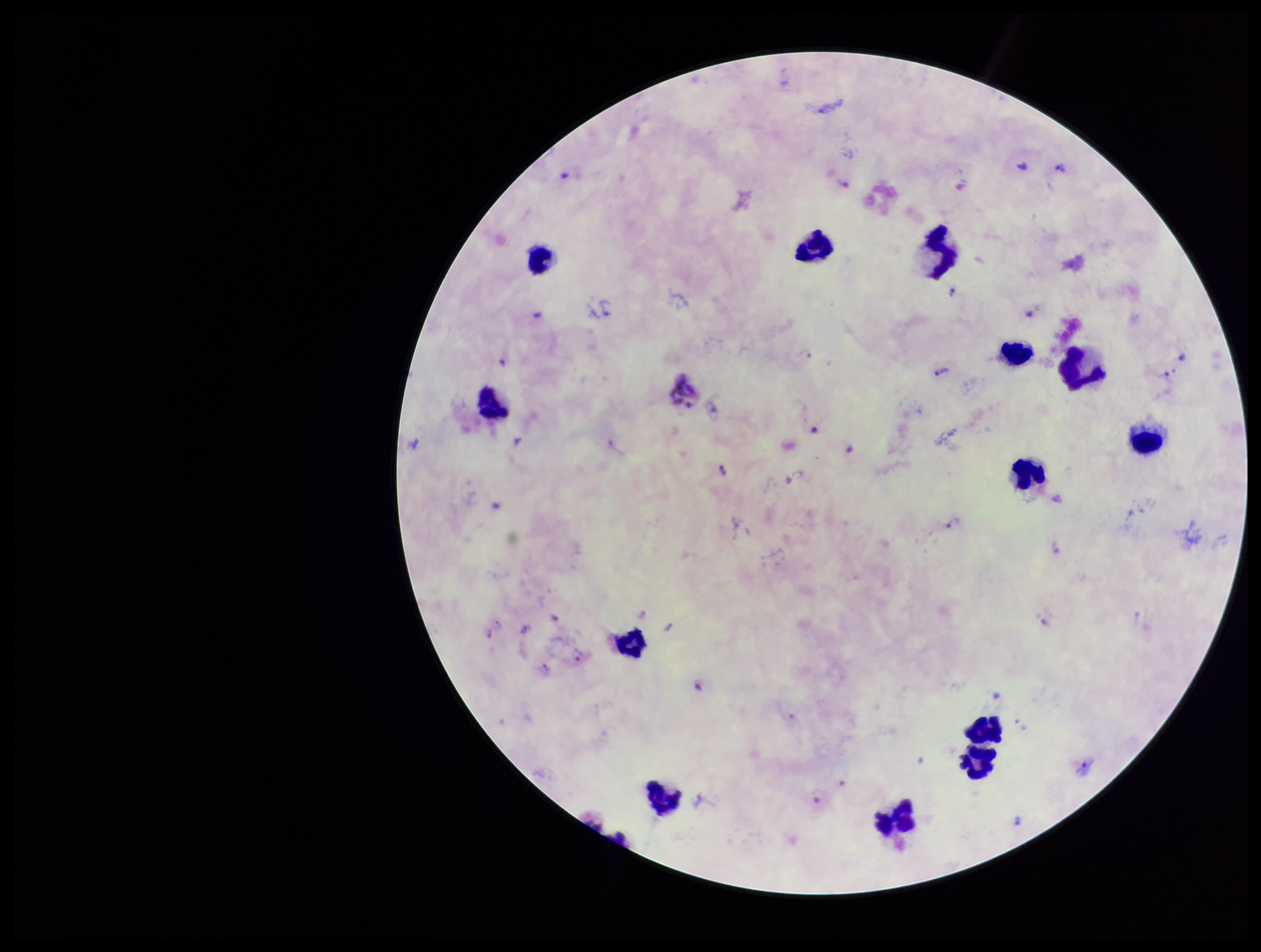
Summary:
  - Stain: Giemsa
  - Capture: smartphone photograph through the microscope eyepiece
  - Image size: 1261×952 pixels
  - Parasite count: 28
  - Preparation: thick blood smear
  - Field of view: single
  - Plasmodium parasites: detected
  - Leukocyte count: 13
  - Patient malaria status: positive
  - Species reported for this patient: Plasmodium vivax